Report the malaria status of this cell.
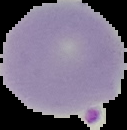
Parasitized.

Image is 127×130 pixels. Cell region segmented out of the field of view; the surrounding area is masked to black. From a thin blood film.